Classify this cell by malaria status.
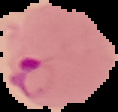

It is parasitized.

Summary:
  - Image size: 118×112 pixels
  - Image type: segmented cell region with the area outside set to black
  - Preparation: thin blood smear